Give the position of every malaria parasite.
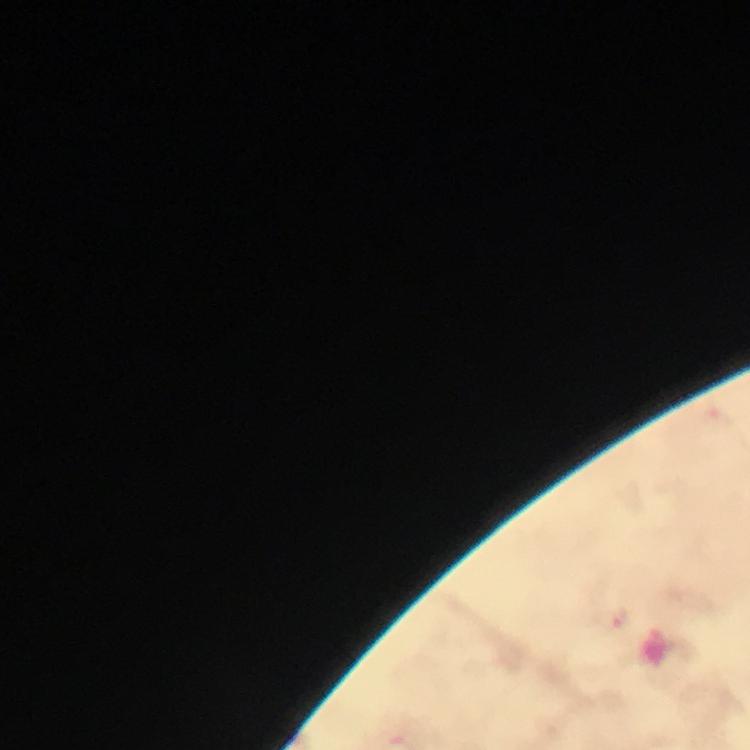

Approximate centers as (x, y) in pixels.
Malaria parasites: (620, 619).

Summary:
  - Context: from a malaria diagnostic workup
  - Capture: smartphone mounted on the microscope
  - Image size: 750×750 pixels
  - Preparation: thick blood smear
  - Cropped from: one field of view
  - Immersion oil: used
  - Magnification: 100x
  - Stain: Giemsa